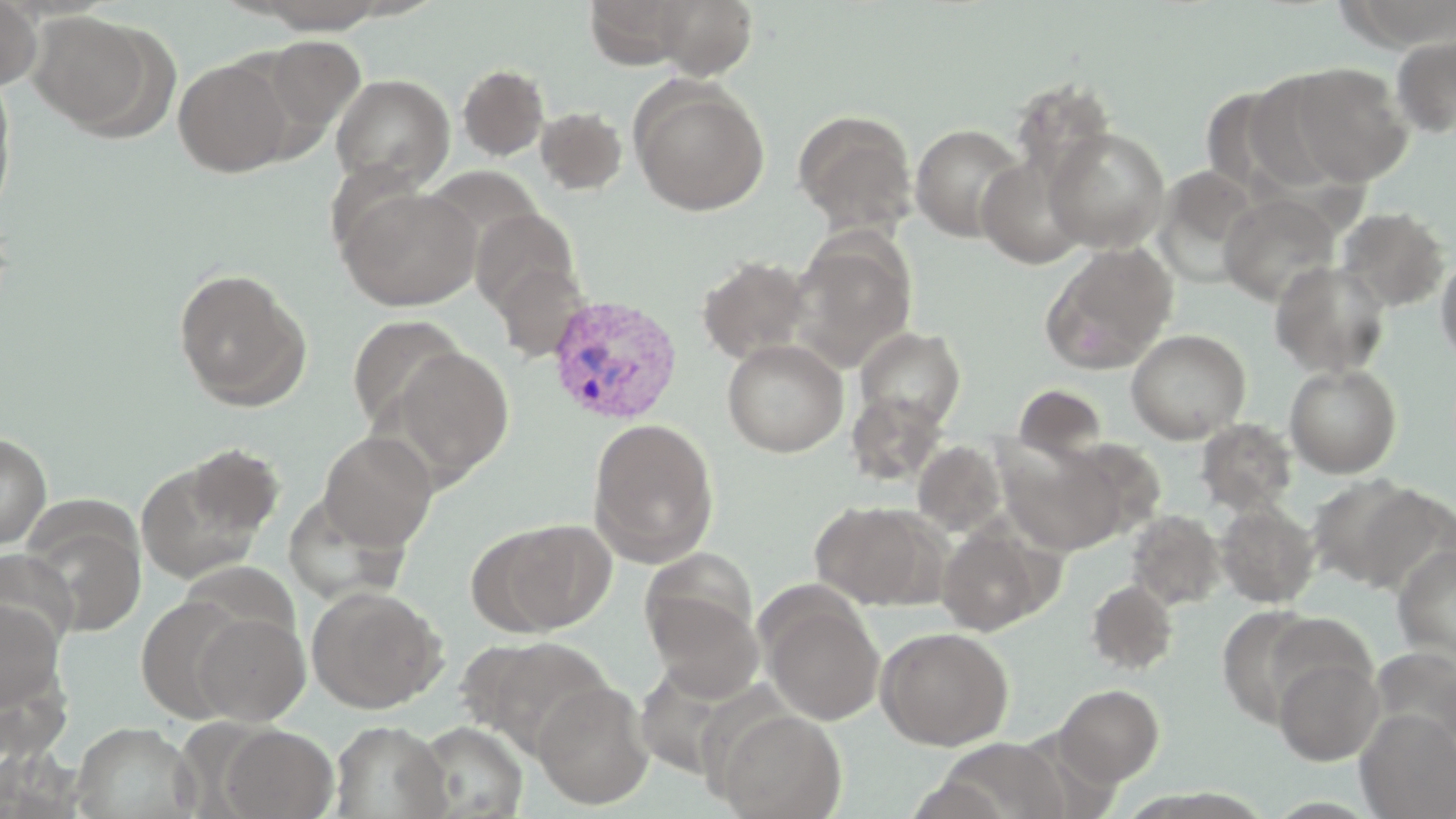
slide-level diagnosis = Plasmodium vivax
image size = 1456×819 pixels
preparation = thin blood smear
Plasmodium vivax-infected red blood cell locations = approximate bounding boxes as [x1, y1, x2, y2] in pixels: [544, 295, 684, 425]
stain = May-Grünwald-Giemsa
modality = light microscopy
uninfected red blood cell locations = approximate bounding boxes as [x1, y1, x2, y2] in pixels: [0, 0, 42, 92], [583, 0, 700, 69], [647, 0, 760, 79], [237, 1, 399, 33], [28, 12, 157, 132], [1391, 34, 1456, 139], [258, 36, 365, 140], [173, 57, 294, 177], [1287, 62, 1414, 186], [457, 63, 550, 160], [0, 73, 16, 220], [330, 73, 454, 192], [1244, 75, 1353, 196], [630, 79, 770, 216], [1010, 80, 1119, 188], [534, 106, 628, 195], [792, 108, 918, 236], [910, 123, 1028, 242], [1043, 126, 1170, 252], [976, 152, 1092, 269], [1154, 166, 1263, 288], [337, 185, 481, 310], [1219, 194, 1340, 306], [1335, 206, 1450, 312], [470, 208, 581, 320], [788, 232, 917, 372], [1040, 242, 1179, 374], [1436, 252, 1456, 366], [695, 255, 814, 365], [490, 258, 591, 363], [1270, 261, 1392, 379], [172, 267, 311, 410], [347, 314, 467, 436], [855, 326, 967, 431], [1126, 328, 1251, 443], [722, 338, 848, 457], [388, 346, 514, 483], [1284, 364, 1402, 477], [1013, 383, 1108, 458], [847, 391, 948, 485], [588, 418, 720, 566], [1196, 418, 1297, 515], [0, 430, 51, 549], [318, 431, 437, 551], [913, 440, 1007, 537], [999, 441, 1126, 555], [135, 451, 279, 585], [1306, 473, 1431, 590], [810, 500, 944, 609], [1215, 501, 1320, 608], [1125, 510, 1225, 610], [23, 516, 148, 637], [481, 518, 615, 635], [936, 521, 1055, 636], [1392, 545, 1456, 664], [0, 549, 78, 654], [1085, 579, 1178, 675], [306, 585, 446, 714], [646, 591, 763, 701], [135, 594, 250, 722], [0, 596, 66, 719], [763, 599, 885, 724], [1263, 611, 1375, 712], [192, 612, 310, 725], [876, 626, 1013, 749], [469, 635, 615, 756], [1272, 655, 1382, 766], [532, 681, 654, 809], [1054, 684, 1165, 786], [715, 709, 847, 818], [1356, 709, 1456, 819], [329, 720, 451, 818], [411, 720, 529, 819], [71, 722, 199, 819], [220, 725, 338, 818], [940, 736, 1075, 819]
magnification = 1000x
field of view = single